Assess the morphology of the red blood cells.
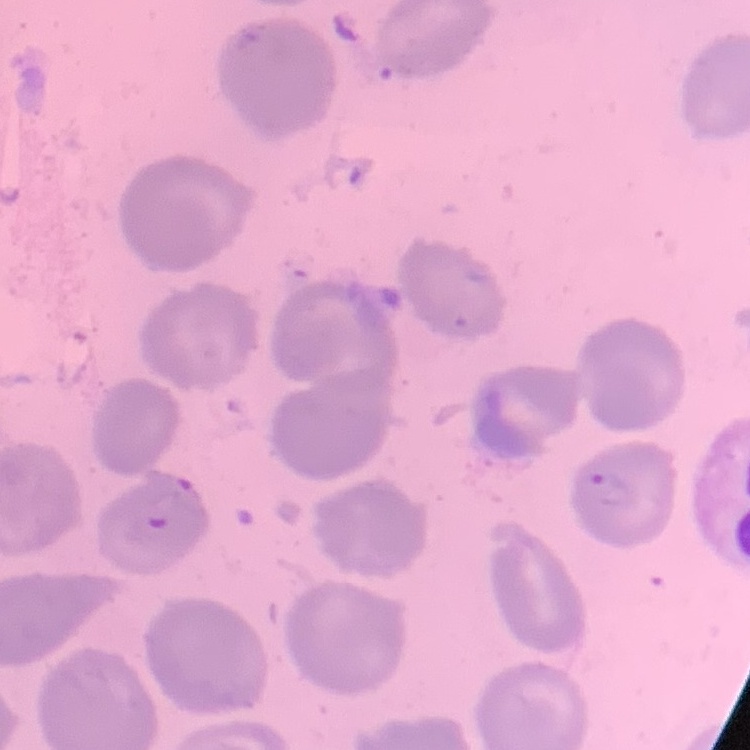

They show no rouleaux formation.

stain: Field's or Giemsa
image_type: square crop of a larger photomicrograph
preparation: thin blood film